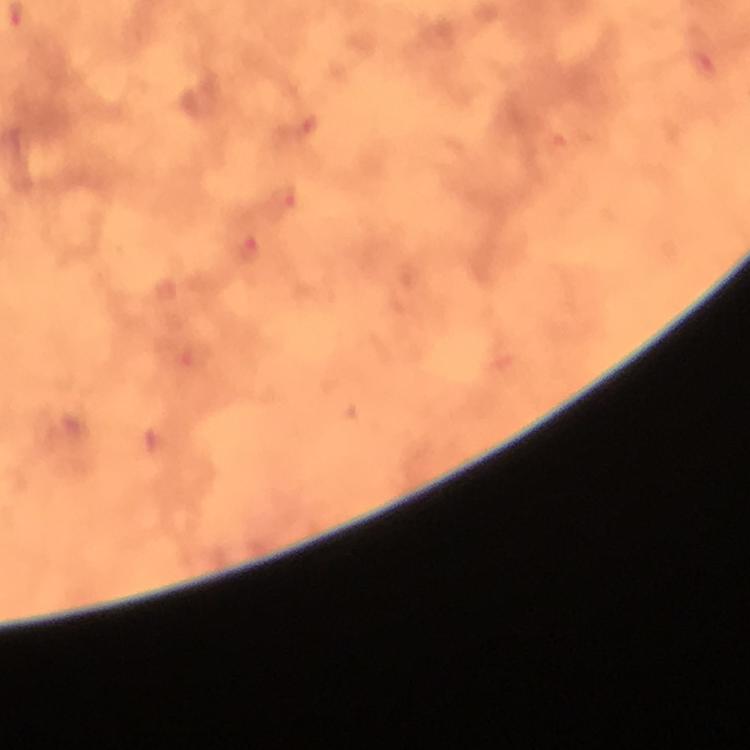
Approximate object centers, in pixels from the top-left corner. Malaria parasite locations: (x=282, y=202), (x=249, y=250). 100x magnification. From a diagnostic examination for malaria. Immersion oil applied. Giemsa stain. Smartphone photograph taken through a microscope. A crop from one field of view. Image is 750×750 pixels. Thick blood smear.